Assess this cell for malaria.
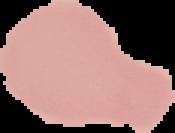
Uninfected.

preparation = thin blood smear
image size = 175×133 pixels
image type = segmented cell region on a black background